Assess this cell for malaria.
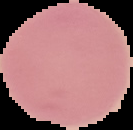

Uninfected.

preparation: thin blood film
image_type: segmented cell region with the area outside set to black
image_size: 133×130 pixels